Identify the blood parasite species.
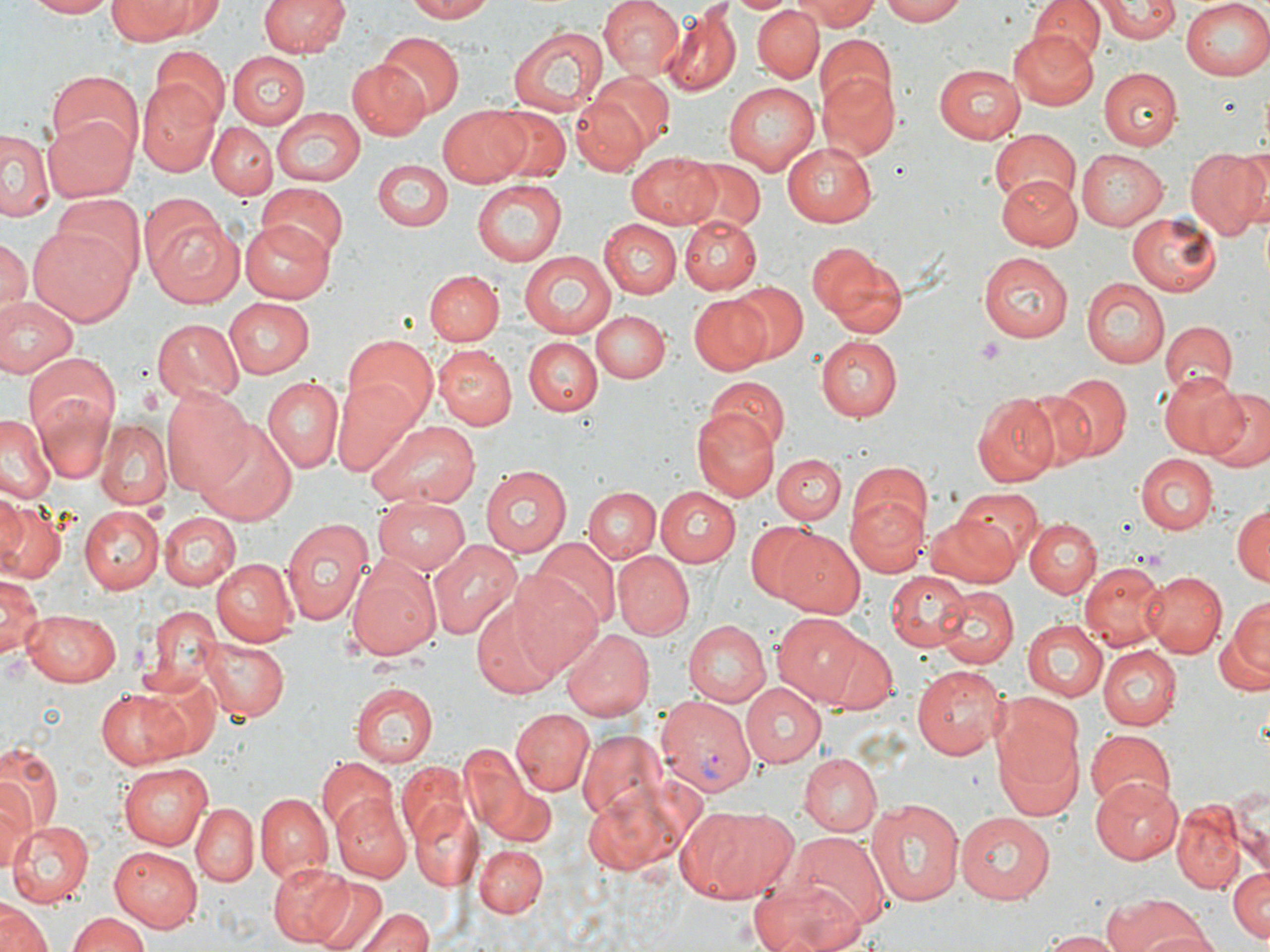
Plasmodium vivax.

uninfected_red_blood_cell_locations: 'approximate bounding boxes as named x1/y1/x2/y2 corners in pixels: (x1=25, y1=0, x2=118, y2=18), (x1=259, y1=0, x2=349, y2=59), (x1=404, y1=0, x2=500, y2=23), (x1=598, y1=0, x2=685, y2=81), (x1=731, y1=0, x2=793, y2=16), (x1=801, y1=0, x2=878, y2=31), (x1=880, y1=0, x2=966, y2=26), (x1=1030, y1=0, x2=1104, y2=64), (x1=1180, y1=0, x2=1270, y2=80), (x1=108, y1=2, x2=198, y2=43), (x1=1098, y1=2, x2=1180, y2=42), (x1=752, y1=5, x2=824, y2=80), (x1=661, y1=6, x2=741, y2=97), (x1=508, y1=24, x2=608, y2=117), (x1=1009, y1=30, x2=1100, y2=111), (x1=375, y1=31, x2=463, y2=119), (x1=815, y1=32, x2=895, y2=114), (x1=149, y1=44, x2=229, y2=128), (x1=226, y1=50, x2=309, y2=127), (x1=346, y1=59, x2=430, y2=141), (x1=933, y1=63, x2=1028, y2=141), (x1=1099, y1=67, x2=1182, y2=150), (x1=46, y1=70, x2=144, y2=157), (x1=818, y1=70, x2=899, y2=161), (x1=585, y1=71, x2=675, y2=151), (x1=137, y1=82, x2=221, y2=175), (x1=723, y1=82, x2=819, y2=174), (x1=570, y1=94, x2=650, y2=177), (x1=438, y1=103, x2=535, y2=185), (x1=271, y1=107, x2=366, y2=185), (x1=490, y1=109, x2=572, y2=185), (x1=42, y1=112, x2=136, y2=202), (x1=208, y1=123, x2=276, y2=198), (x1=990, y1=128, x2=1081, y2=209), (x1=3, y1=130, x2=57, y2=224), (x1=782, y1=141, x2=877, y2=226), (x1=1183, y1=146, x2=1270, y2=242), (x1=1076, y1=149, x2=1168, y2=231), (x1=626, y1=150, x2=722, y2=229), (x1=375, y1=158, x2=452, y2=232), (x1=682, y1=160, x2=765, y2=232), (x1=995, y1=175, x2=1082, y2=248), (x1=472, y1=179, x2=566, y2=266), (x1=256, y1=182, x2=348, y2=261), (x1=53, y1=195, x2=146, y2=281), (x1=1126, y1=211, x2=1222, y2=298), (x1=149, y1=215, x2=246, y2=308), (x1=679, y1=215, x2=761, y2=293), (x1=241, y1=219, x2=333, y2=304), (x1=598, y1=220, x2=682, y2=299), (x1=27, y1=224, x2=135, y2=326), (x1=2, y1=237, x2=30, y2=316), (x1=807, y1=241, x2=904, y2=337), (x1=517, y1=251, x2=620, y2=340), (x1=979, y1=252, x2=1071, y2=343), (x1=427, y1=270, x2=503, y2=344), (x1=1082, y1=276, x2=1171, y2=369), (x1=728, y1=281, x2=810, y2=364), (x1=688, y1=295, x2=771, y2=374), (x1=0, y1=296, x2=80, y2=381), (x1=221, y1=297, x2=312, y2=380), (x1=589, y1=309, x2=669, y2=384), (x1=152, y1=319, x2=243, y2=403), (x1=1160, y1=320, x2=1236, y2=396), (x1=341, y1=336, x2=438, y2=426), (x1=523, y1=336, x2=603, y2=416), (x1=816, y1=337, x2=902, y2=420), (x1=435, y1=345, x2=518, y2=429), (x1=23, y1=354, x2=121, y2=449), (x1=1155, y1=371, x2=1247, y2=459), (x1=1057, y1=374, x2=1131, y2=459), (x1=263, y1=375, x2=342, y2=472), (x1=330, y1=375, x2=425, y2=476), (x1=704, y1=375, x2=790, y2=456), (x1=1020, y1=382, x2=1115, y2=470), (x1=161, y1=383, x2=255, y2=496), (x1=1202, y1=389, x2=1270, y2=470), (x1=972, y1=393, x2=1061, y2=486), (x1=33, y1=396, x2=116, y2=487), (x1=691, y1=408, x2=779, y2=502), (x1=0, y1=416, x2=57, y2=504), (x1=197, y1=419, x2=298, y2=525), (x1=365, y1=420, x2=480, y2=511), (x1=95, y1=421, x2=171, y2=510), (x1=773, y1=453, x2=844, y2=524), (x1=1134, y1=454, x2=1218, y2=534), (x1=848, y1=463, x2=933, y2=543), (x1=481, y1=465, x2=572, y2=556), (x1=656, y1=485, x2=743, y2=567), (x1=583, y1=487, x2=660, y2=563), (x1=950, y1=488, x2=1040, y2=571), (x1=847, y1=491, x2=929, y2=577), (x1=0, y1=495, x2=28, y2=573), (x1=372, y1=496, x2=469, y2=572), (x1=0, y1=503, x2=67, y2=584), (x1=77, y1=505, x2=163, y2=593), (x1=1230, y1=505, x2=1268, y2=586), (x1=157, y1=512, x2=240, y2=591), (x1=926, y1=512, x2=1023, y2=586), (x1=282, y1=518, x2=374, y2=627), (x1=1026, y1=518, x2=1101, y2=598), (x1=745, y1=520, x2=830, y2=605), (x1=773, y1=530, x2=865, y2=617), (x1=427, y1=539, x2=520, y2=640), (x1=533, y1=539, x2=621, y2=629), (x1=614, y1=552, x2=694, y2=641), (x1=210, y1=556, x2=297, y2=645), (x1=346, y1=556, x2=441, y2=662), (x1=1079, y1=562, x2=1164, y2=647), (x1=1140, y1=569, x2=1227, y2=658), (x1=883, y1=570, x2=976, y2=652), (x1=0, y1=572, x2=41, y2=663), (x1=511, y1=574, x2=607, y2=680), (x1=934, y1=587, x2=1018, y2=671), (x1=1223, y1=593, x2=1269, y2=688), (x1=468, y1=594, x2=566, y2=699), (x1=141, y1=604, x2=221, y2=694), (x1=23, y1=610, x2=121, y2=686), (x1=775, y1=615, x2=877, y2=706), (x1=1022, y1=619, x2=1107, y2=702), (x1=682, y1=621, x2=770, y2=707), (x1=561, y1=629, x2=655, y2=721), (x1=807, y1=631, x2=898, y2=714), (x1=202, y1=637, x2=288, y2=722), (x1=1098, y1=647, x2=1181, y2=730), (x1=912, y1=663, x2=1007, y2=758), (x1=134, y1=672, x2=221, y2=762), (x1=350, y1=681, x2=437, y2=766), (x1=739, y1=682, x2=827, y2=766), (x1=95, y1=689, x2=190, y2=769), (x1=510, y1=709, x2=594, y2=796), (x1=991, y1=719, x2=1086, y2=822), (x1=1084, y1=728, x2=1178, y2=813), (x1=579, y1=730, x2=670, y2=823), (x1=458, y1=742, x2=533, y2=837), (x1=0, y1=743, x2=61, y2=838), (x1=799, y1=753, x2=883, y2=837), (x1=316, y1=759, x2=398, y2=840), (x1=119, y1=763, x2=213, y2=848), (x1=398, y1=763, x2=467, y2=842), (x1=581, y1=775, x2=706, y2=881), (x1=1090, y1=778, x2=1183, y2=862), (x1=0, y1=784, x2=35, y2=872), (x1=484, y1=784, x2=555, y2=848), (x1=1229, y1=784, x2=1269, y2=876), (x1=256, y1=792, x2=332, y2=882), (x1=331, y1=793, x2=412, y2=882), (x1=865, y1=798, x2=966, y2=909), (x1=411, y1=799, x2=481, y2=893), (x1=1171, y1=801, x2=1246, y2=893), (x1=193, y1=804, x2=258, y2=886), (x1=674, y1=805, x2=800, y2=901), (x1=955, y1=813, x2=1056, y2=902), (x1=10, y1=819, x2=95, y2=906), (x1=786, y1=834, x2=888, y2=932), (x1=477, y1=845, x2=546, y2=917), (x1=108, y1=846, x2=203, y2=932), (x1=267, y1=861, x2=353, y2=946), (x1=1227, y1=865, x2=1270, y2=940), (x1=746, y1=876, x2=868, y2=952), (x1=309, y1=877, x2=387, y2=951), (x1=1100, y1=892, x2=1208, y2=952), (x1=1, y1=902, x2=51, y2=952), (x1=358, y1=908, x2=434, y2=952), (x1=66, y1=912, x2=150, y2=952), (x1=1039, y1=930, x2=1126, y2=951)'
plasmodium_vivax_infected_red_blood_cell_locations: 'approximate bounding boxes as named x1/y1/x2/y2 corners in pixels: (x1=652, y1=694, x2=757, y2=792)'
field_of_view: one of a larger specimen
modality: optical microscopy
platelet_locations: 'approximate bounding boxes as named x1/y1/x2/y2 corners in pixels: (x1=976, y1=337, x2=1006, y2=365)'
image_size: 1270×952 pixels
stain: May-Grünwald-Giemsa
magnification: 1000x
preparation: thin blood smear